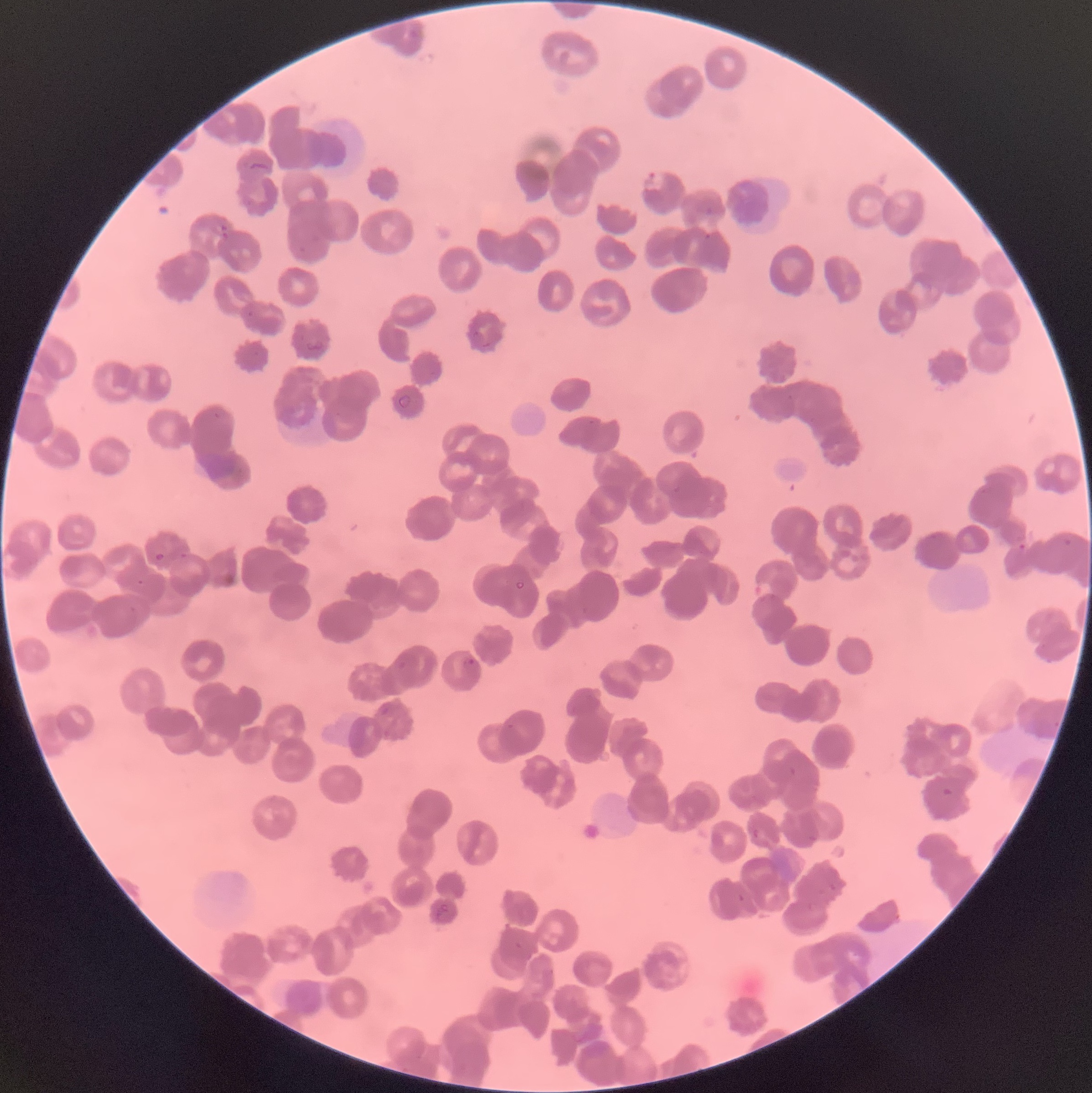

Summary:
  - Coordinate format: approximate bounding boxes as [x1, y1, x2, y2] in pixels
  - Plasmodium parasite locations: [640, 171, 667, 192], [215, 225, 229, 239], [1018, 538, 1026, 551], [1063, 539, 1072, 546], [153, 553, 166, 562], [136, 579, 144, 586], [464, 658, 480, 675], [394, 660, 407, 670], [507, 723, 516, 730], [940, 785, 955, 797], [751, 828, 766, 842], [516, 943, 532, 962]
  - Plasmodium parasites too small for a box (approximate centers as [x, y] in pixels): [249, 314]
  - Modality: optical microscopy
  - Red blood cell morphology: rouleaux formation
  - Image size: 1092×1093 pixels
  - Preparation: thin blood film